Locate and identify every blood parasite.
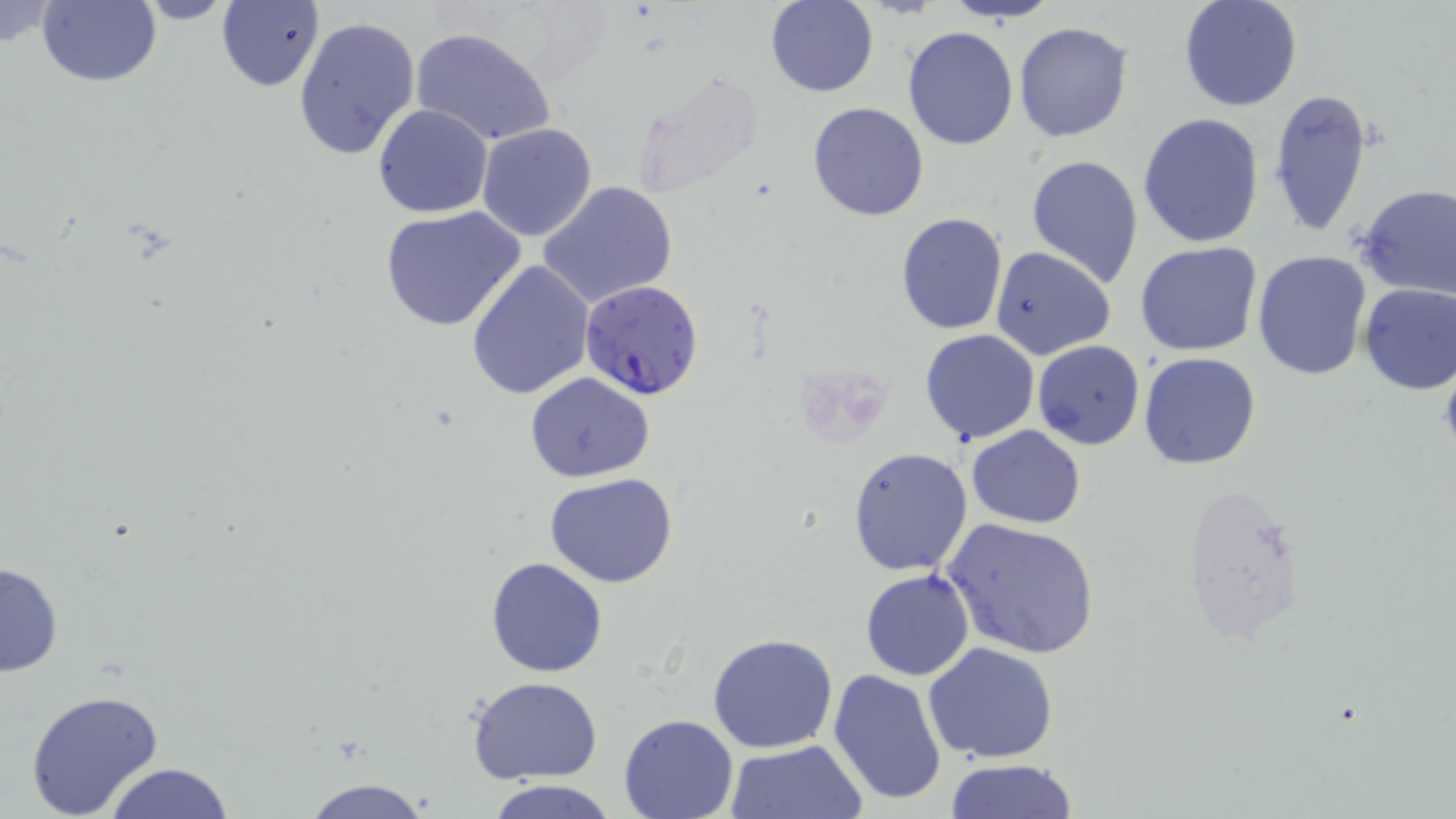
Approximate bounding boxes as named x1/y1/x2/y2 corners in pixels.
Plasmodium falciparum-infected red blood cells: (x1=580, y1=278, x2=705, y2=399).
No Plasmodium ovale, Plasmodium malariae, Plasmodium vivax, Babesia divergens, or Trypanosoma brucei observed.

slide-level diagnosis = Plasmodium falciparum
preparation = thin blood film
uninfected red blood cell locations = approximate bounding boxes as named x1/y1/x2/y2 corners in pixels: (x1=0, y1=0, x2=62, y2=53), (x1=38, y1=0, x2=161, y2=87), (x1=132, y1=0, x2=236, y2=26), (x1=947, y1=0, x2=1058, y2=23), (x1=1178, y1=0, x2=1303, y2=113), (x1=765, y1=1, x2=880, y2=97), (x1=216, y1=2, x2=325, y2=91), (x1=292, y1=16, x2=421, y2=162), (x1=1013, y1=21, x2=1133, y2=142), (x1=901, y1=25, x2=1018, y2=150), (x1=408, y1=26, x2=558, y2=148), (x1=630, y1=71, x2=766, y2=200), (x1=1268, y1=89, x2=1374, y2=238), (x1=807, y1=102, x2=929, y2=221), (x1=373, y1=104, x2=493, y2=218), (x1=1137, y1=112, x2=1266, y2=250), (x1=476, y1=122, x2=597, y2=241), (x1=1027, y1=153, x2=1144, y2=288), (x1=538, y1=180, x2=679, y2=308), (x1=1357, y1=182, x2=1455, y2=300), (x1=380, y1=205, x2=527, y2=333), (x1=896, y1=211, x2=1007, y2=333), (x1=1133, y1=241, x2=1261, y2=356), (x1=990, y1=246, x2=1117, y2=361), (x1=1253, y1=249, x2=1373, y2=380), (x1=467, y1=258, x2=596, y2=399), (x1=1356, y1=283, x2=1456, y2=395), (x1=918, y1=330, x2=1040, y2=445), (x1=1032, y1=340, x2=1145, y2=450), (x1=1138, y1=352, x2=1263, y2=469), (x1=524, y1=373, x2=655, y2=481), (x1=966, y1=425, x2=1087, y2=528), (x1=846, y1=446, x2=973, y2=577), (x1=545, y1=471, x2=678, y2=588), (x1=1182, y1=484, x2=1306, y2=649), (x1=941, y1=518, x2=1100, y2=660), (x1=485, y1=556, x2=609, y2=677), (x1=0, y1=559, x2=63, y2=678), (x1=860, y1=568, x2=975, y2=680), (x1=707, y1=631, x2=839, y2=754), (x1=921, y1=642, x2=1062, y2=765), (x1=827, y1=668, x2=949, y2=807), (x1=465, y1=677, x2=604, y2=783), (x1=24, y1=689, x2=167, y2=818), (x1=618, y1=713, x2=740, y2=819), (x1=725, y1=738, x2=868, y2=819), (x1=945, y1=758, x2=1080, y2=817), (x1=103, y1=762, x2=236, y2=819), (x1=292, y1=777, x2=440, y2=818), (x1=482, y1=779, x2=626, y2=818)
image size = 1456×819 pixels
modality = light microscopy
field of view = one of a larger specimen
stain = May-Grünwald-Giemsa
magnification = 1000x